Assess the morphology of the erythrocytes.
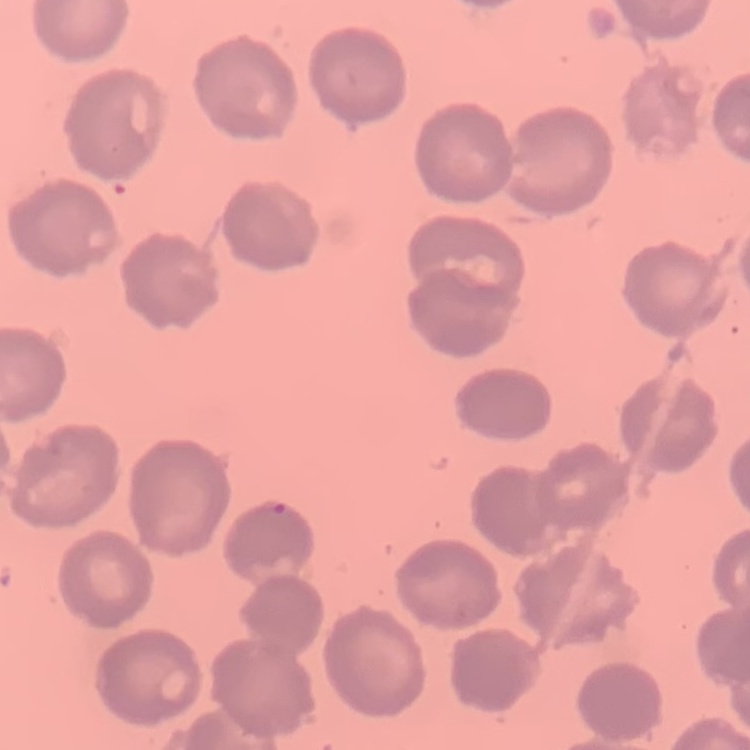

They show no rouleaux formation.

image_type: one tile cut from a larger photomicrograph
stain: Field's or Giemsa
preparation: thin peripheral smear